Give the position of every leukocyte visible.
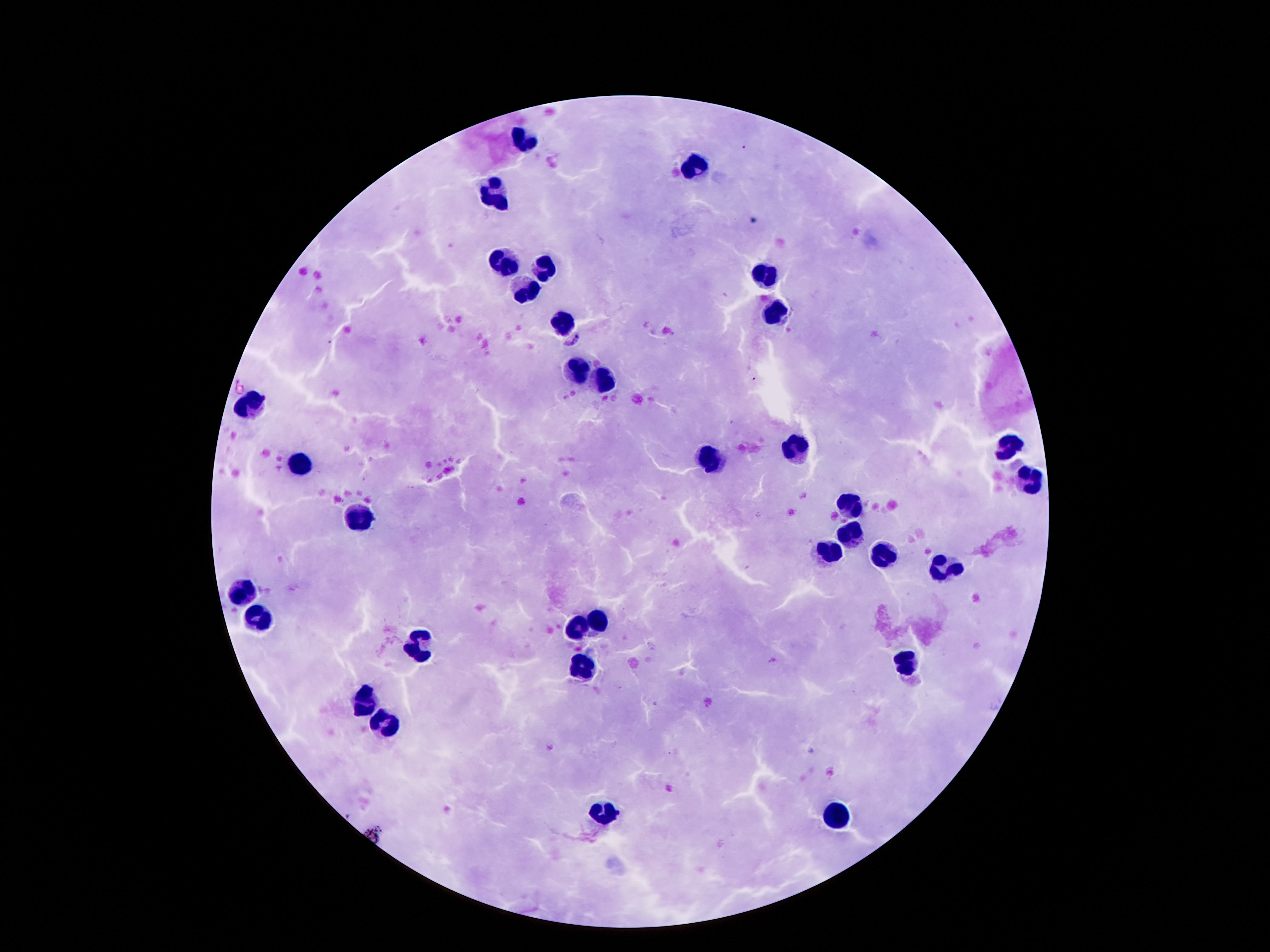
Approximate centers as {x, y} in pixels.
Leukocytes: {528, 137}, {698, 169}, {493, 191}, {502, 260}, {545, 266}, {764, 278}, {526, 292}, {776, 315}, {565, 325}, {578, 372}, {610, 385}, {252, 405}, {1005, 448}, {795, 450}, {711, 460}, {299, 461}, {1026, 481}, {848, 507}, {365, 514}, {850, 534}, {827, 548}, {883, 555}, {944, 569}, {242, 592}, {258, 619}, {600, 623}, {578, 627}, {414, 642}, {580, 664}, {907, 664}, {367, 703}, {389, 723}, {835, 814}, {604, 815}.

Smartphone photograph taken through the microscope eyepiece. Giemsa stain. Image is 1270×952 pixels. Patient malaria status: uninfected. 100x magnification. Thick blood film. One field from this slide.